Locate every malaria parasite.
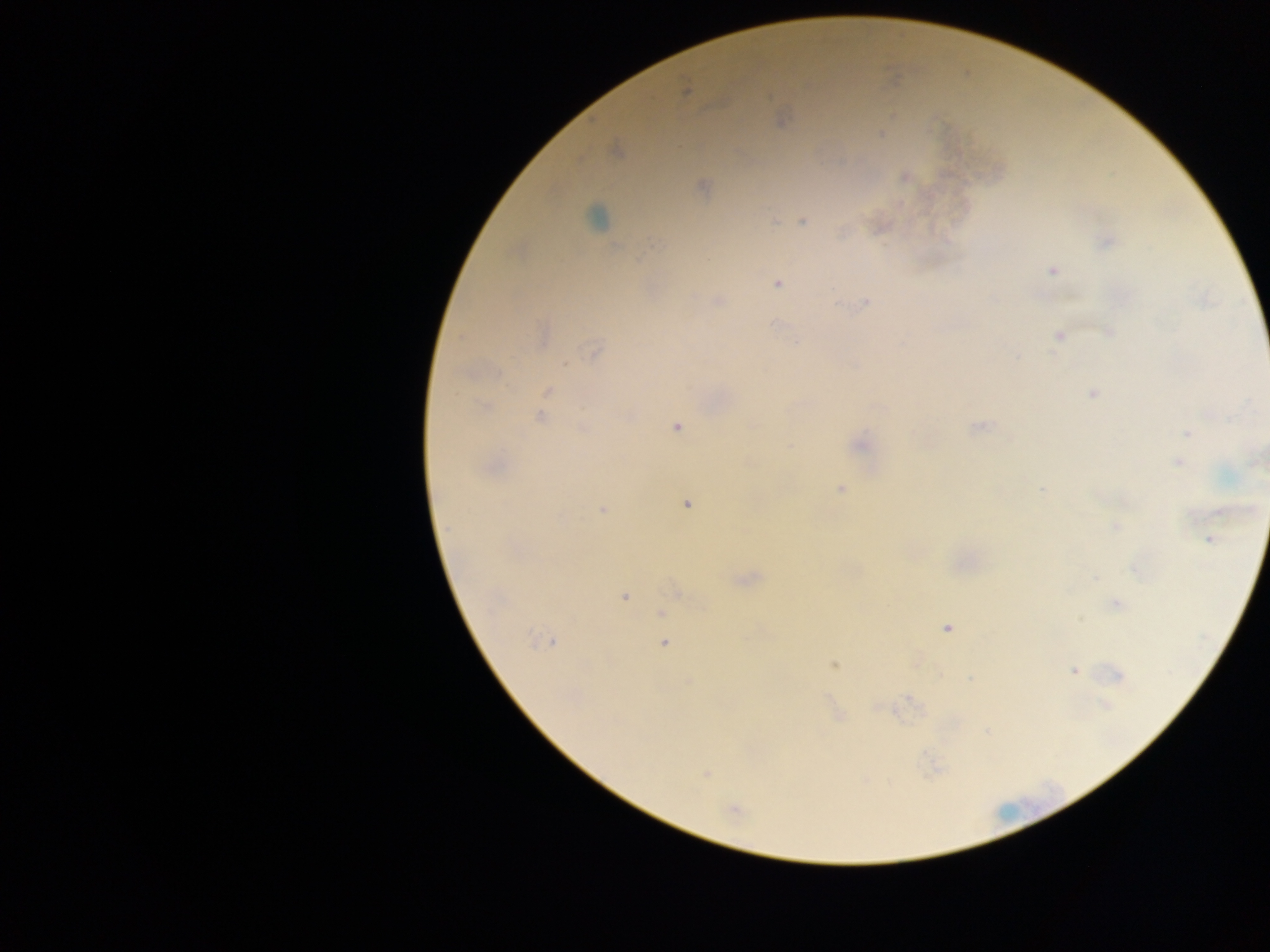
Approximate centers as {x, y} in pixels.
Malaria parasites: {685, 91}, {780, 119}, {881, 135}, {616, 150}, {905, 177}, {702, 187}, {597, 217}, {803, 221}, {1107, 242}, {1052, 270}, {777, 283}, {718, 300}, {866, 301}, {1109, 330}, {1059, 336}, {542, 337}, {797, 342}, {594, 350}, {547, 391}, {1091, 392}, {484, 406}, {539, 416}, {978, 425}, {677, 426}, {582, 427}, {1187, 433}, {858, 443}, {1179, 461}, {490, 468}, {839, 488}, {1042, 488}, {686, 503}, {603, 510}, {1116, 527}, {1211, 540}, {1136, 567}, {745, 579}, {677, 591}, {624, 597}, {1115, 603}, {662, 612}, {947, 628}, {543, 641}, {664, 643}, {917, 661}, {834, 664}, {1074, 670}, {1116, 675}, {971, 678}, {910, 699}, {883, 708}, {838, 715}, {988, 732}, {705, 773}, {733, 808}.

Summary:
  - Preparation: thick blood smear
  - Country: Ghana
  - Capture: mobile-phone photograph through a microscope
  - Image size: 1270×952 pixels
  - Field of view: single